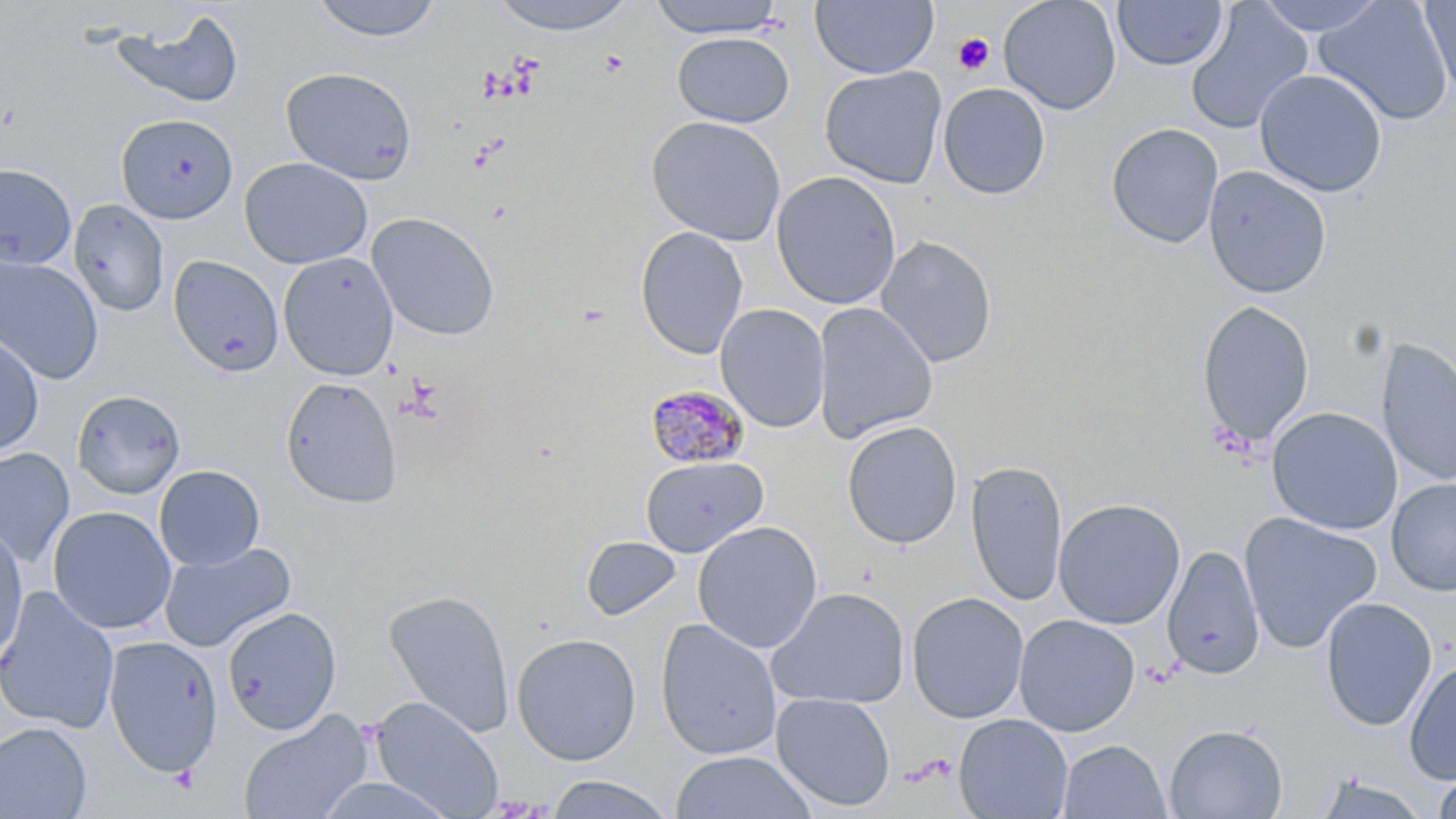
slide-level diagnosis = Plasmodium malariae
modality = light microscopy
Plasmodium malariae-infected red blood cell locations = approximate bounding boxes as (x1,y1)-(x2,y2) corner pairs in pixels: (645,383)-(751,470)
uninfected red blood cell locations = approximate bounding boxes as (x1,y1)-(x2,y2) corner pairs in pixels: (308,0)-(445,43), (485,0)-(643,36), (646,0)-(789,39), (812,0)-(938,79), (998,0)-(1122,115), (1112,0)-(1228,71), (1254,0)-(1387,35), (1313,0)-(1453,126), (1418,0)-(1455,97), (1186,2)-(1313,135), (113,10)-(244,113), (672,32)-(795,127), (280,66)-(417,184), (819,66)-(948,189), (1254,69)-(1387,197), (937,82)-(1051,200), (116,114)-(237,224), (647,115)-(787,246), (1106,122)-(1224,249), (239,157)-(373,269), (0,163)-(77,270), (1203,165)-(1332,299), (771,171)-(902,310), (69,198)-(169,317), (366,211)-(500,341), (635,226)-(749,360), (875,235)-(998,368), (278,252)-(398,380), (0,255)-(104,384), (168,255)-(284,377), (1195,300)-(1315,448), (813,302)-(938,444), (715,303)-(830,433), (0,331)-(44,459), (1376,337)-(1456,488), (280,376)-(402,508), (72,390)-(185,500), (1266,406)-(1402,535), (842,420)-(962,549), (0,448)-(75,567), (640,455)-(769,557), (965,460)-(1068,606), (154,464)-(265,570), (1386,477)-(1456,596), (1052,498)-(1186,630), (47,506)-(176,634), (1239,511)-(1382,654), (692,520)-(823,654), (0,523)-(28,665), (581,536)-(683,622), (159,541)-(296,652), (1162,545)-(1264,679), (0,586)-(119,734), (767,586)-(910,709), (382,589)-(516,739), (906,591)-(1030,724), (1319,596)-(1437,731), (222,607)-(341,735), (1013,614)-(1140,736), (655,618)-(782,761), (511,632)-(641,765), (103,636)-(222,778), (1404,659)-(1456,784), (771,692)-(896,812), (371,697)-(503,817), (237,709)-(373,819), (954,713)-(1073,819), (0,722)-(92,819), (1164,723)-(1288,818), (1058,739)-(1170,819), (669,750)-(816,819), (1432,765)-(1456,819), (313,774)-(461,819), (545,775)-(675,817), (1314,775)-(1432,819)
image size = 1456×819 pixels
preparation = thin blood smear
stain = May-Grünwald-Giemsa
platelet locations = approximate bounding boxes as (x1,y1)-(x2,y2) corner pairs in pixels: (952,32)-(995,76)
magnification = 1000x
field of view = single